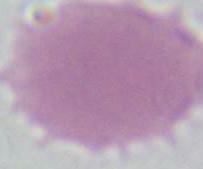

Summary:
  - Modality: micrograph
  - Magnification: 1000x
  - Identification: red blood cell